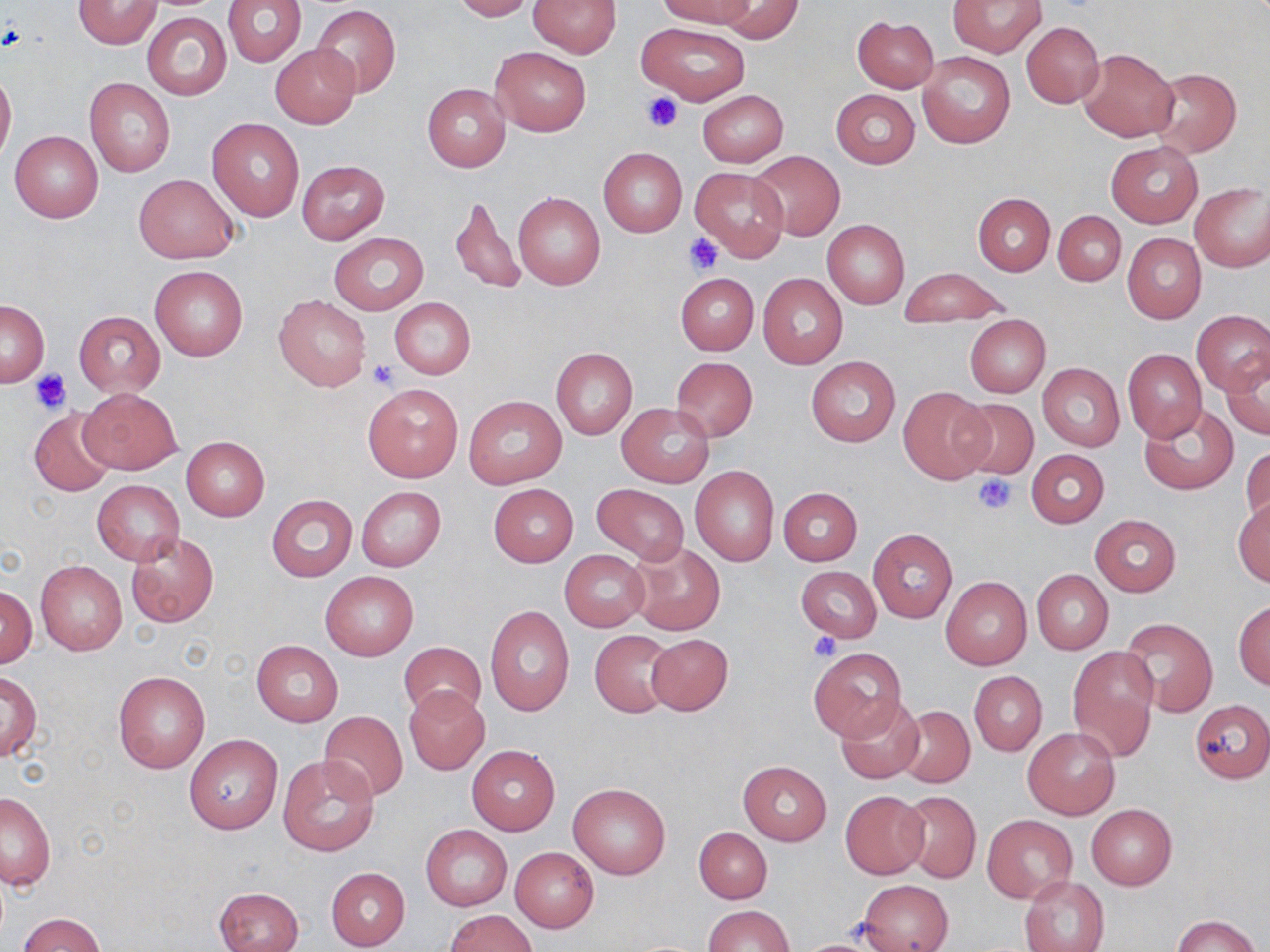
Summary:
  - Coordinate format: approximate bounding boxes as named x1/y1/x2/y2 corners in pixels
  - Platelet locations: (x1=642, y1=93, x2=684, y2=134), (x1=683, y1=233, x2=723, y2=275), (x1=368, y1=360, x2=399, y2=390), (x1=30, y1=369, x2=70, y2=413), (x1=971, y1=473, x2=1017, y2=515), (x1=808, y1=631, x2=840, y2=662)
  - Uninfected red blood cell locations: (x1=73, y1=0, x2=160, y2=48), (x1=223, y1=0, x2=305, y2=67), (x1=451, y1=0, x2=536, y2=21), (x1=527, y1=0, x2=621, y2=57), (x1=657, y1=0, x2=757, y2=30), (x1=718, y1=0, x2=802, y2=43), (x1=949, y1=0, x2=1046, y2=56), (x1=312, y1=4, x2=401, y2=97), (x1=142, y1=12, x2=232, y2=101), (x1=852, y1=16, x2=939, y2=93), (x1=636, y1=21, x2=750, y2=105), (x1=1021, y1=22, x2=1104, y2=106), (x1=270, y1=44, x2=360, y2=127), (x1=490, y1=47, x2=591, y2=136), (x1=1078, y1=48, x2=1179, y2=141), (x1=917, y1=51, x2=1015, y2=148), (x1=0, y1=68, x2=16, y2=162), (x1=1149, y1=68, x2=1241, y2=157), (x1=84, y1=78, x2=175, y2=177), (x1=422, y1=84, x2=511, y2=171), (x1=830, y1=89, x2=920, y2=166), (x1=697, y1=90, x2=789, y2=166), (x1=207, y1=118, x2=304, y2=222), (x1=10, y1=131, x2=104, y2=223), (x1=1105, y1=140, x2=1202, y2=228), (x1=598, y1=147, x2=687, y2=238), (x1=749, y1=150, x2=845, y2=240), (x1=297, y1=160, x2=389, y2=244), (x1=691, y1=166, x2=789, y2=261), (x1=135, y1=173, x2=238, y2=264), (x1=1190, y1=183, x2=1270, y2=272), (x1=513, y1=192, x2=605, y2=291), (x1=450, y1=193, x2=526, y2=296), (x1=973, y1=193, x2=1055, y2=275), (x1=1052, y1=211, x2=1125, y2=285), (x1=822, y1=219, x2=910, y2=310), (x1=329, y1=232, x2=428, y2=315), (x1=1122, y1=232, x2=1206, y2=324), (x1=150, y1=265, x2=247, y2=360), (x1=900, y1=269, x2=1007, y2=325), (x1=675, y1=273, x2=758, y2=354), (x1=758, y1=273, x2=848, y2=369), (x1=274, y1=295, x2=371, y2=392), (x1=389, y1=297, x2=475, y2=380), (x1=1, y1=299, x2=48, y2=386), (x1=1192, y1=310, x2=1270, y2=394), (x1=74, y1=312, x2=165, y2=396), (x1=964, y1=313, x2=1051, y2=397), (x1=551, y1=348, x2=636, y2=439), (x1=1122, y1=349, x2=1207, y2=442), (x1=806, y1=356, x2=901, y2=446), (x1=1223, y1=356, x2=1270, y2=439), (x1=670, y1=357, x2=758, y2=442), (x1=1037, y1=363, x2=1125, y2=451), (x1=362, y1=382, x2=463, y2=483), (x1=898, y1=386, x2=994, y2=484), (x1=79, y1=388, x2=181, y2=475), (x1=463, y1=396, x2=567, y2=488), (x1=953, y1=398, x2=1039, y2=481), (x1=1140, y1=401, x2=1239, y2=494), (x1=617, y1=404, x2=714, y2=487), (x1=28, y1=407, x2=117, y2=497), (x1=180, y1=436, x2=269, y2=522), (x1=1241, y1=443, x2=1269, y2=527), (x1=1026, y1=449, x2=1109, y2=528), (x1=690, y1=465, x2=779, y2=566), (x1=92, y1=480, x2=184, y2=564), (x1=488, y1=484, x2=578, y2=566), (x1=592, y1=484, x2=689, y2=565), (x1=356, y1=487, x2=445, y2=571), (x1=779, y1=487, x2=862, y2=566), (x1=266, y1=494, x2=358, y2=581), (x1=1232, y1=498, x2=1270, y2=588), (x1=1090, y1=515, x2=1182, y2=597), (x1=868, y1=529, x2=957, y2=622), (x1=125, y1=532, x2=218, y2=627), (x1=628, y1=542, x2=725, y2=635), (x1=559, y1=550, x2=649, y2=631), (x1=36, y1=559, x2=127, y2=655), (x1=796, y1=565, x2=881, y2=642), (x1=1032, y1=569, x2=1113, y2=654), (x1=321, y1=572, x2=418, y2=660), (x1=940, y1=576, x2=1031, y2=670), (x1=1, y1=587, x2=37, y2=666), (x1=1234, y1=600, x2=1270, y2=689), (x1=485, y1=604, x2=574, y2=719), (x1=1119, y1=617, x2=1219, y2=718), (x1=590, y1=629, x2=677, y2=717), (x1=646, y1=633, x2=732, y2=714), (x1=251, y1=640, x2=343, y2=727), (x1=399, y1=641, x2=486, y2=721), (x1=809, y1=648, x2=907, y2=742), (x1=1068, y1=649, x2=1159, y2=761), (x1=113, y1=671, x2=210, y2=774), (x1=970, y1=671, x2=1047, y2=756), (x1=1, y1=672, x2=41, y2=762), (x1=405, y1=686, x2=489, y2=774), (x1=836, y1=697, x2=925, y2=784), (x1=1189, y1=699, x2=1270, y2=783), (x1=894, y1=705, x2=975, y2=789), (x1=320, y1=711, x2=408, y2=801), (x1=1023, y1=727, x2=1120, y2=820), (x1=183, y1=734, x2=282, y2=834), (x1=466, y1=744, x2=560, y2=834), (x1=276, y1=754, x2=379, y2=857), (x1=738, y1=759, x2=832, y2=845), (x1=569, y1=782, x2=670, y2=880), (x1=840, y1=791, x2=929, y2=879), (x1=897, y1=791, x2=981, y2=883), (x1=1, y1=792, x2=56, y2=888), (x1=1085, y1=804, x2=1176, y2=890), (x1=983, y1=815, x2=1076, y2=901), (x1=420, y1=824, x2=512, y2=911), (x1=694, y1=827, x2=773, y2=904), (x1=510, y1=847, x2=599, y2=931), (x1=326, y1=867, x2=409, y2=951), (x1=1021, y1=875, x2=1109, y2=952), (x1=859, y1=879, x2=953, y2=952), (x1=214, y1=886, x2=303, y2=952), (x1=702, y1=904, x2=794, y2=952), (x1=447, y1=910, x2=535, y2=952), (x1=19, y1=913, x2=106, y2=952), (x1=1169, y1=914, x2=1263, y2=952)
  - Slide-level diagnosis: negative for blood parasites
  - Preparation: thin blood film
  - Stain: May-Grünwald-Giemsa
  - Modality: light microscopy
  - Field of view: one of a larger specimen
  - Image size: 1270×952 pixels
  - Magnification: 1000x